Name the parasite shown.
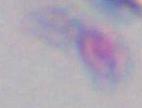
This is Toxoplasma gondii.

{
  "modality": "micrograph",
  "magnification": "1000x"
}